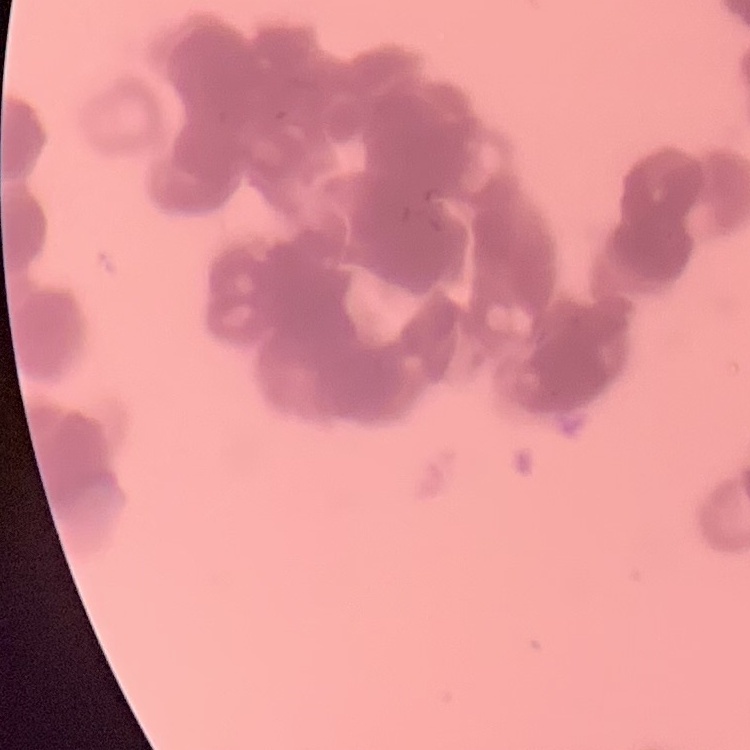

Summary:
  - Red blood cell morphology: rouleaux formation
  - Image type: one tile cut from a larger photomicrograph
  - Preparation: thin blood smear
  - Stain: Field's or Giemsa